Give the extent of all Plasmodium vivax-infected red blood cells.
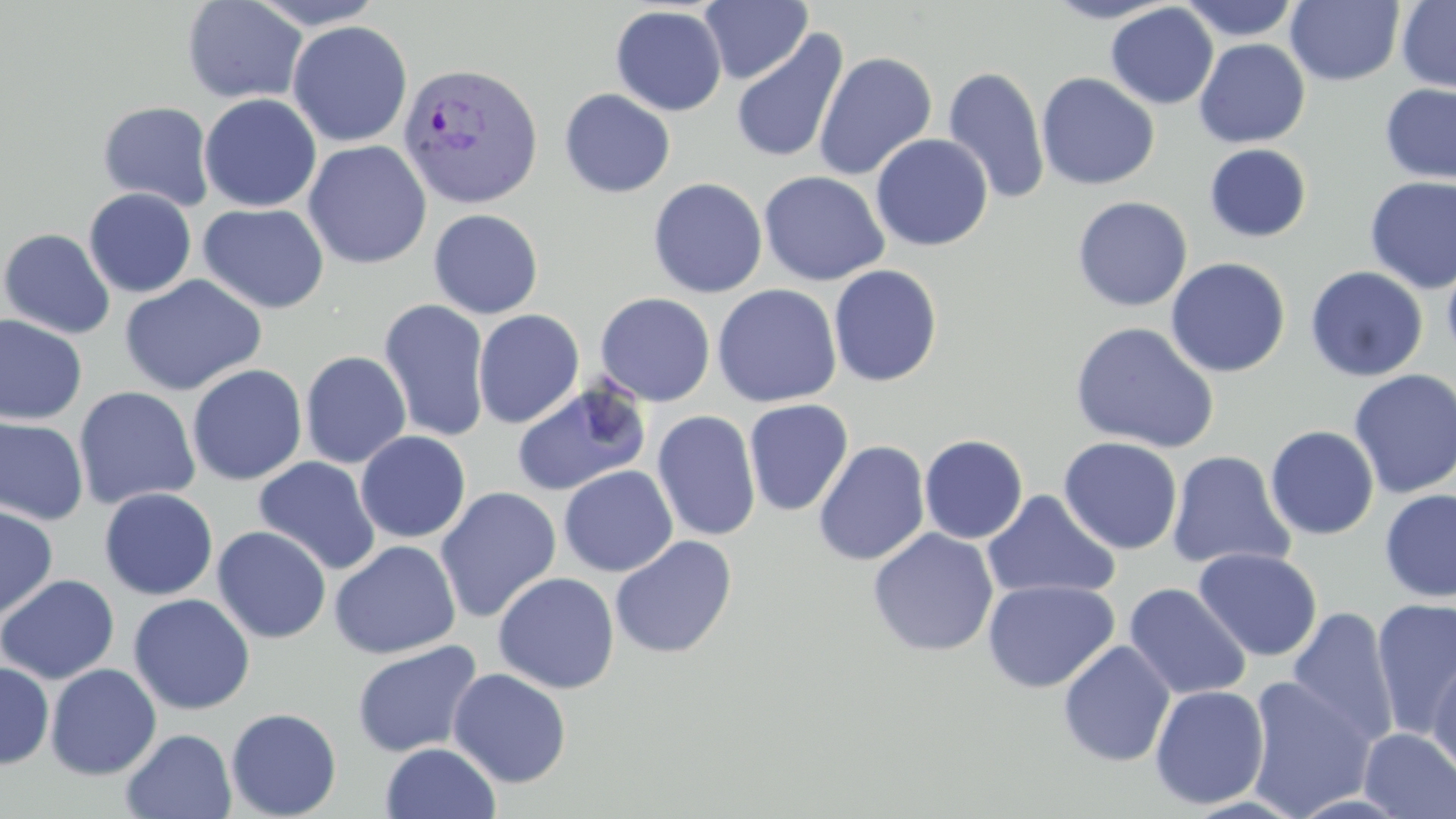
Approximate bounding boxes as (x1,y1)-(x2,y2) corner pairs in pixels.
Plasmodium vivax-infected red blood cells: (397,61)-(544,210).

Uninfected red blood cell locations: (182,0)-(308,104), (249,0)-(385,28), (699,0)-(812,84), (1043,0)-(1177,23), (1179,0)-(1302,42), (1286,0)-(1404,86), (1396,0)-(1456,94), (1105,4)-(1219,109), (610,5)-(728,116), (287,20)-(412,147), (730,29)-(850,165), (1193,39)-(1310,148), (813,51)-(938,181), (942,66)-(1051,204), (1036,72)-(1160,190), (1379,83)-(1456,185), (559,88)-(676,198), (198,93)-(322,213), (98,101)-(215,211), (870,133)-(993,251), (303,140)-(432,269), (1204,143)-(1312,243), (758,170)-(889,286), (1364,176)-(1456,294), (648,177)-(768,299), (83,188)-(197,297), (1072,196)-(1193,311), (198,203)-(329,314), (428,208)-(543,319), (0,228)-(115,339), (1441,247)-(1456,368), (1165,258)-(1291,378), (828,264)-(943,387), (1305,266)-(1428,382), (119,275)-(267,396), (712,284)-(842,407), (595,292)-(716,407), (378,299)-(491,442), (473,309)-(584,428), (0,314)-(87,426), (1069,321)-(1219,453), (300,351)-(411,469), (187,364)-(308,485), (1348,368)-(1456,499), (511,377)-(652,497), (73,386)-(200,509), (743,399)-(854,516), (652,410)-(762,542), (0,416)-(90,526), (1265,425)-(1379,540), (355,431)-(471,543), (919,434)-(1029,544), (1058,436)-(1183,554), (813,440)-(930,566), (1166,451)-(1295,571), (253,456)-(381,576), (559,466)-(678,577), (434,486)-(562,624), (99,488)-(218,600), (982,489)-(1121,602), (1378,489)-(1455,603), (0,504)-(58,622), (212,526)-(331,644), (867,528)-(999,657), (610,535)-(737,659), (329,540)-(461,660), (1192,547)-(1322,662), (493,572)-(620,694), (0,574)-(120,685), (983,578)-(1120,694), (1123,582)-(1252,701), (128,593)-(255,715), (1370,598)-(1456,738), (1286,607)-(1400,750), (1057,639)-(1176,767), (352,640)-(483,757), (1428,656)-(1456,781), (0,661)-(54,769), (45,663)-(162,780), (448,668)-(572,789), (1244,675)-(1377,818), (1149,684)-(1270,810), (226,707)-(342,819), (121,728)-(237,818), (1359,728)-(1456,819), (380,742)-(501,819). Slide-level diagnosis: Plasmodium vivax. Thin blood film. One field of a larger specimen. Light microscopy. Captured at 1000x magnification. May-Grünwald-Giemsa stain. Image is 1456×819 pixels.